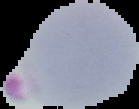
image size = 139×109 pixels
preparation = thin blood smear
result = Plasmodium parasites identified
image type = segmented cell region on a black background